Locate every blood parasite and identify its species.
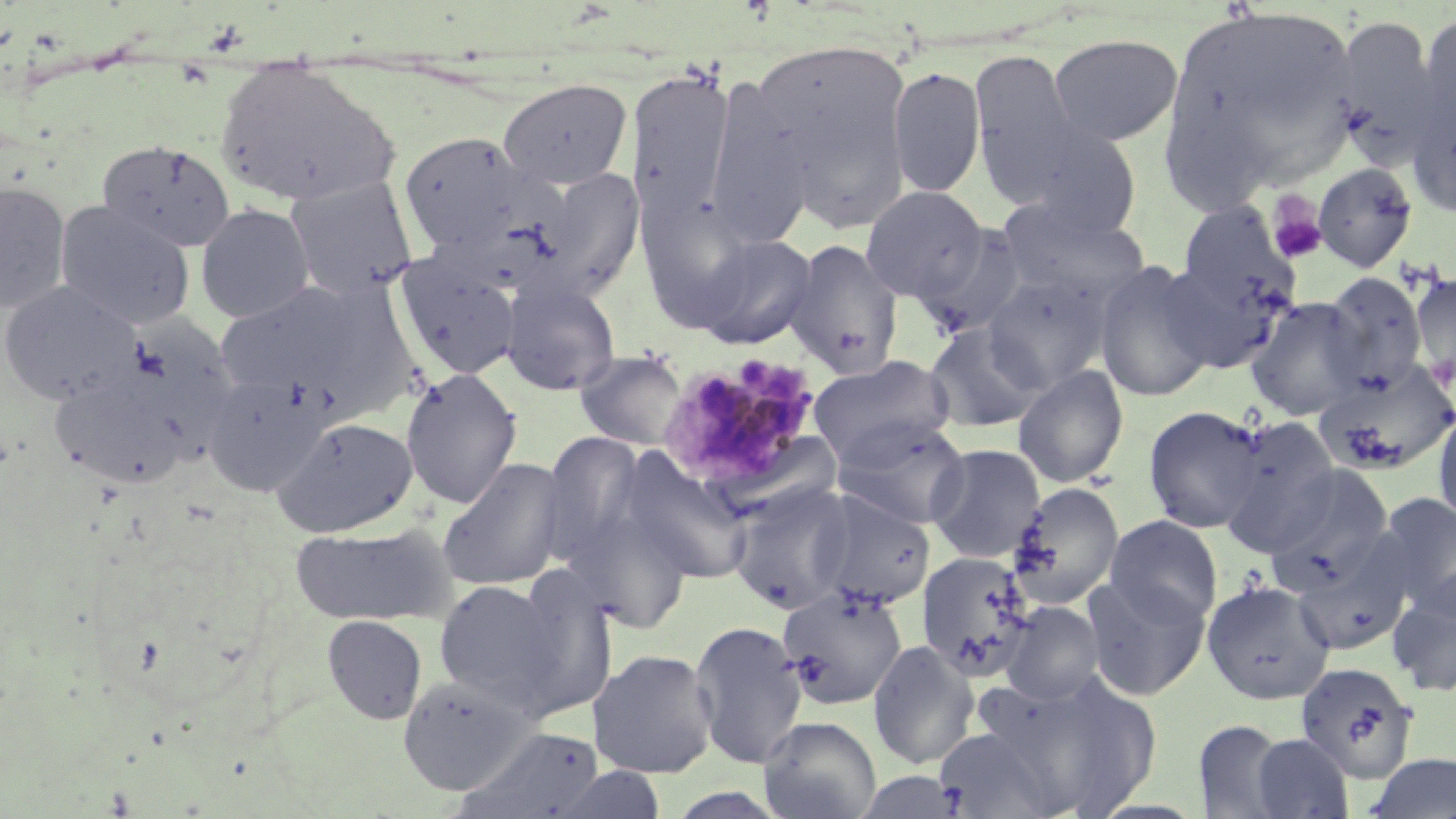

Approximate bounding boxes as named x1/y1/x2/y2 corners in pixels.
Plasmodium malariae-infected red blood cells: (x1=657, y1=353, x2=826, y2=495).
No Plasmodium falciparum, Plasmodium ovale, Plasmodium vivax, Babesia divergens, or Trypanosoma brucei observed.

Summary:
  - Platelet locations: (x1=1264, y1=191, x2=1328, y2=265)
  - Uninfected red blood cell locations: (x1=1161, y1=5, x2=1363, y2=193), (x1=1416, y1=12, x2=1456, y2=144), (x1=1331, y1=15, x2=1446, y2=166), (x1=1048, y1=34, x2=1182, y2=146), (x1=750, y1=36, x2=915, y2=215), (x1=968, y1=50, x2=1086, y2=197), (x1=213, y1=59, x2=399, y2=209), (x1=626, y1=65, x2=736, y2=227), (x1=887, y1=66, x2=986, y2=199), (x1=701, y1=78, x2=818, y2=248), (x1=498, y1=79, x2=633, y2=190), (x1=1407, y1=80, x2=1456, y2=221), (x1=1010, y1=118, x2=1143, y2=238), (x1=399, y1=130, x2=539, y2=258), (x1=97, y1=139, x2=236, y2=252), (x1=1311, y1=162, x2=1419, y2=272), (x1=515, y1=165, x2=646, y2=301), (x1=284, y1=177, x2=420, y2=300), (x1=0, y1=181, x2=71, y2=314), (x1=859, y1=185, x2=989, y2=303), (x1=996, y1=199, x2=1150, y2=311), (x1=55, y1=202, x2=196, y2=330), (x1=1175, y1=202, x2=1302, y2=320), (x1=194, y1=203, x2=315, y2=324), (x1=913, y1=223, x2=1034, y2=339), (x1=692, y1=232, x2=818, y2=349), (x1=783, y1=239, x2=904, y2=378), (x1=1156, y1=254, x2=1294, y2=374), (x1=395, y1=257, x2=522, y2=381), (x1=1092, y1=260, x2=1217, y2=402), (x1=1409, y1=270, x2=1455, y2=391), (x1=981, y1=271, x2=1112, y2=394), (x1=1320, y1=271, x2=1429, y2=393), (x1=500, y1=278, x2=622, y2=396), (x1=0, y1=280, x2=141, y2=406), (x1=213, y1=283, x2=363, y2=398), (x1=291, y1=284, x2=425, y2=421), (x1=1245, y1=296, x2=1370, y2=421), (x1=923, y1=322, x2=1047, y2=434), (x1=573, y1=349, x2=690, y2=452), (x1=808, y1=354, x2=957, y2=471), (x1=47, y1=361, x2=197, y2=489), (x1=1314, y1=362, x2=1456, y2=476), (x1=1013, y1=364, x2=1129, y2=488), (x1=400, y1=368, x2=521, y2=509), (x1=200, y1=370, x2=330, y2=495), (x1=1431, y1=403, x2=1456, y2=532), (x1=1142, y1=405, x2=1270, y2=534), (x1=271, y1=415, x2=419, y2=539), (x1=1217, y1=417, x2=1344, y2=556), (x1=833, y1=418, x2=971, y2=530), (x1=539, y1=431, x2=649, y2=562), (x1=542, y1=437, x2=718, y2=605), (x1=926, y1=443, x2=1047, y2=564), (x1=619, y1=452, x2=755, y2=586), (x1=436, y1=456, x2=570, y2=592), (x1=1259, y1=463, x2=1396, y2=596), (x1=728, y1=481, x2=858, y2=616), (x1=1007, y1=482, x2=1125, y2=609), (x1=810, y1=490, x2=936, y2=612), (x1=1370, y1=491, x2=1456, y2=618), (x1=557, y1=503, x2=694, y2=633), (x1=1105, y1=514, x2=1223, y2=627), (x1=289, y1=523, x2=453, y2=626), (x1=1291, y1=545, x2=1412, y2=657), (x1=918, y1=551, x2=1039, y2=683), (x1=501, y1=569, x2=619, y2=717), (x1=1386, y1=572, x2=1456, y2=699), (x1=1082, y1=575, x2=1211, y2=702), (x1=432, y1=579, x2=566, y2=709), (x1=1202, y1=579, x2=1335, y2=705), (x1=777, y1=586, x2=909, y2=710), (x1=1000, y1=601, x2=1106, y2=705), (x1=322, y1=615, x2=427, y2=724), (x1=688, y1=620, x2=809, y2=768), (x1=867, y1=639, x2=979, y2=769), (x1=590, y1=648, x2=718, y2=779), (x1=1294, y1=661, x2=1419, y2=785), (x1=982, y1=671, x2=1163, y2=818), (x1=397, y1=673, x2=534, y2=794), (x1=758, y1=716, x2=882, y2=819), (x1=1191, y1=718, x2=1291, y2=818), (x1=460, y1=725, x2=606, y2=819), (x1=933, y1=726, x2=1071, y2=818), (x1=1250, y1=733, x2=1355, y2=818), (x1=1362, y1=753, x2=1456, y2=819), (x1=553, y1=765, x2=667, y2=819), (x1=853, y1=771, x2=970, y2=818)
  - Slide-level diagnosis: Plasmodium malariae
  - Stain: May-Grünwald-Giemsa
  - Modality: light microscopy
  - Field of view: one of a larger specimen
  - Image size: 1456×819 pixels
  - Magnification: 1000x
  - Preparation: thin blood film